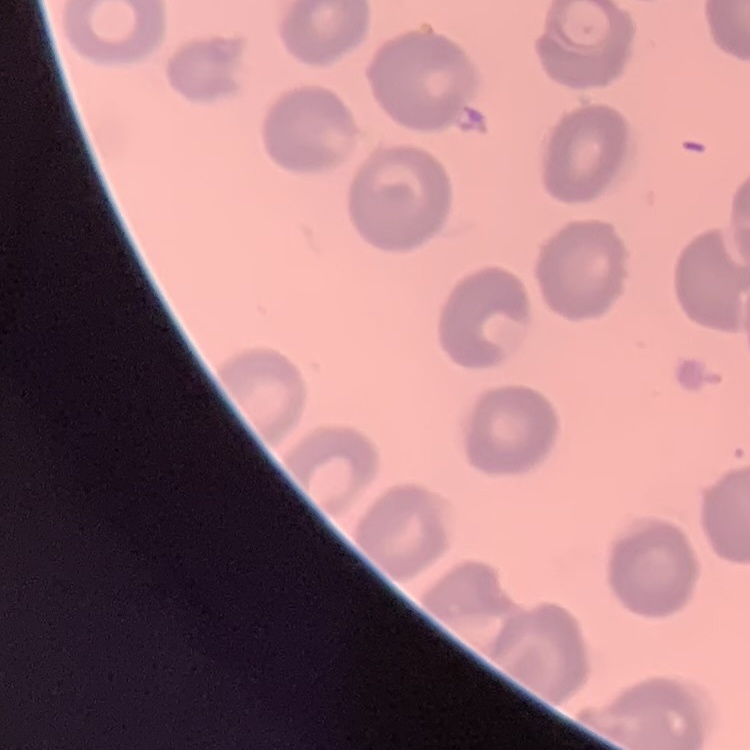

Summary:
  - Erythrocyte morphology: no rouleaux formation
  - Stain: Field's or Giemsa
  - Preparation: thin peripheral smear
  - Image type: square crop of a larger photomicrograph